Report the malaria status of this cell.
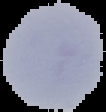

It is uninfected.

From a thin blood film. Image is 106×112 pixels. The area outside the segmented cell region is set to black.